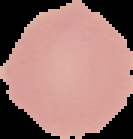
Summary:
  - Image type: cell region segmented out of the field of view; surrounding area masked to black
  - Preparation: thin blood film
  - Image size: 133×139 pixels
  - Malaria status: uninfected